Classify this cell by malaria status.
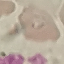

It is uninfected.

Thin blood smear. Acquired by smartphone through the microscope eyepiece. Giemsa stain. Automatically extracted cell patch, resized to 64 × 64 pixels.